Identify the parasite.
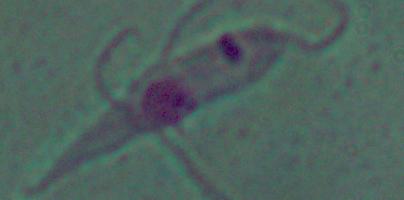
This is Leishmania.

modality = micrograph
magnification = 1000x